Report the malaria status of this cell.
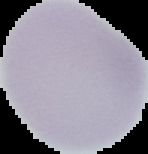
Uninfected.

preparation: thin blood smear
image_type: segmented cell region on a black background
image_size: 148×154 pixels